Outline each uninfected red blood cell.
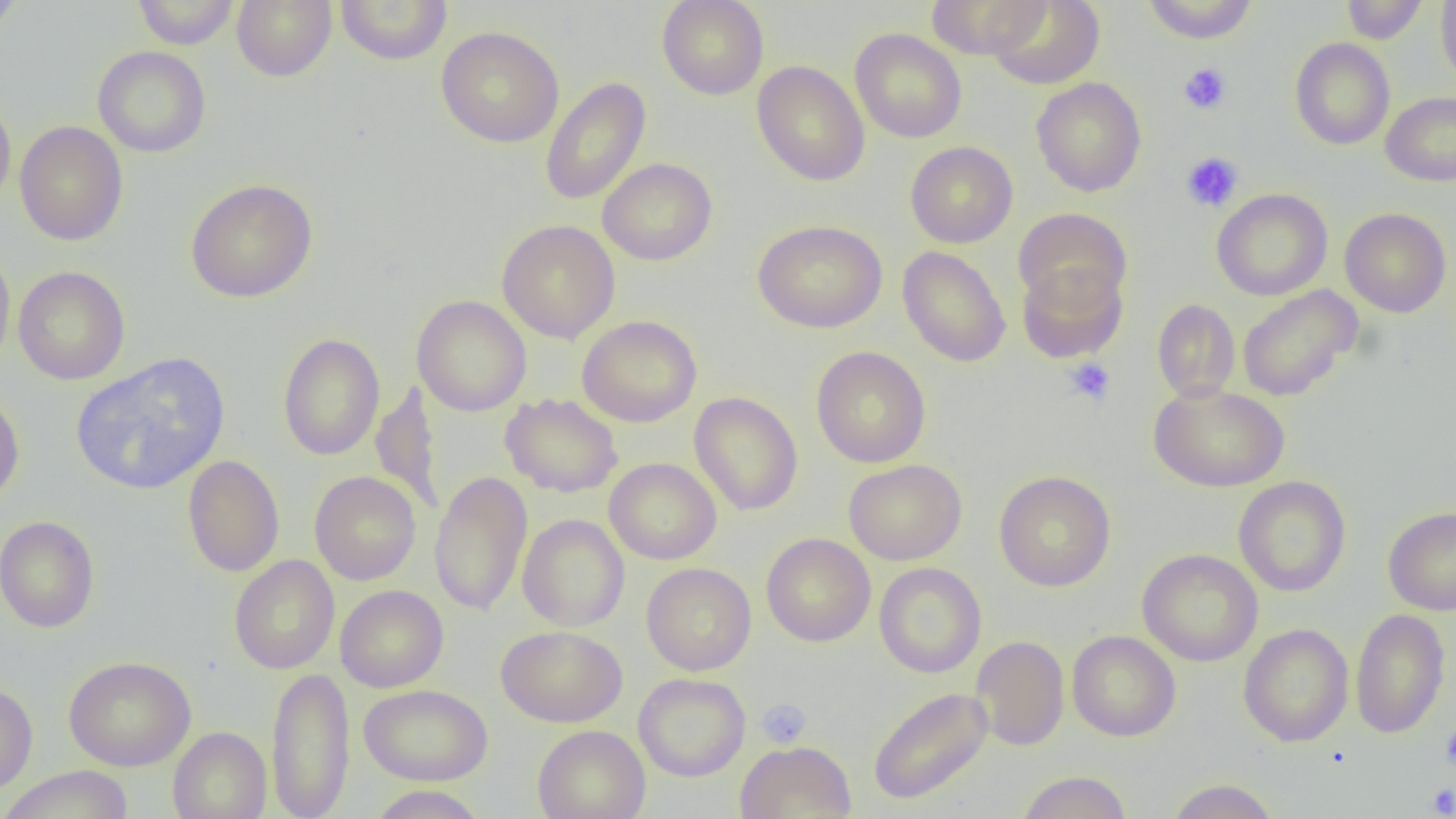

Approximate bounding boxes as (x1, y1, x2, y2) in pixels.
Uninfected red blood cells: (0, 0, 25, 36), (132, 0, 239, 49), (232, 0, 336, 82), (335, 0, 453, 65), (657, 0, 769, 100), (925, 0, 1052, 58), (987, 0, 1105, 90), (1142, 0, 1258, 44), (1341, 0, 1428, 44), (1435, 0, 1456, 85), (436, 26, 564, 148), (849, 28, 966, 143), (1289, 37, 1395, 150), (92, 46, 211, 158), (751, 60, 870, 186), (539, 77, 651, 206), (1031, 77, 1146, 197), (1380, 91, 1456, 186), (0, 94, 16, 211), (14, 120, 128, 246), (905, 141, 1018, 248), (598, 158, 717, 266), (185, 178, 318, 303), (1212, 188, 1332, 300), (1340, 207, 1452, 318), (1013, 208, 1131, 314), (496, 219, 620, 344), (752, 219, 887, 333), (0, 245, 15, 374), (897, 246, 1011, 367), (1016, 262, 1128, 364), (12, 266, 130, 385), (1237, 284, 1362, 402), (412, 295, 532, 416), (1152, 298, 1240, 402), (577, 315, 702, 427), (277, 333, 385, 461), (811, 346, 931, 468), (71, 353, 230, 495), (370, 381, 444, 516), (1149, 383, 1290, 492), (0, 388, 25, 508), (688, 392, 803, 516), (501, 393, 622, 498), (182, 455, 285, 577), (604, 457, 722, 564), (843, 459, 967, 565), (429, 470, 532, 616), (994, 470, 1116, 591), (309, 471, 421, 585), (1233, 476, 1351, 597), (1383, 506, 1456, 616), (517, 514, 629, 631), (0, 515, 100, 633), (761, 533, 876, 647), (1137, 549, 1263, 667), (229, 555, 340, 674), (642, 562, 756, 676), (874, 563, 986, 678), (335, 585, 448, 692), (1350, 608, 1450, 739), (1238, 623, 1354, 747), (496, 625, 627, 727), (1067, 630, 1181, 741), (971, 636, 1069, 750), (63, 655, 196, 771), (266, 665, 355, 819), (634, 673, 750, 781), (0, 682, 38, 797), (359, 684, 492, 785), (867, 686, 993, 806), (532, 725, 650, 819), (168, 727, 271, 819), (734, 741, 856, 819), (0, 766, 135, 819), (1017, 770, 1131, 819), (1165, 779, 1279, 818), (367, 785, 489, 818).

Summary:
  - Platelet locations: (1179, 63, 1232, 114), (1180, 152, 1243, 212), (1063, 358, 1116, 406), (756, 697, 812, 748), (1439, 723, 1456, 772), (1426, 783, 1455, 817)
  - Slide-level diagnosis: no evidence of blood parasites
  - Image size: 1456×819 pixels
  - Modality: optical microscopy
  - Field of view: one of a larger specimen
  - Magnification: 1000x
  - Preparation: thin blood smear